Identify the blood parasite species.
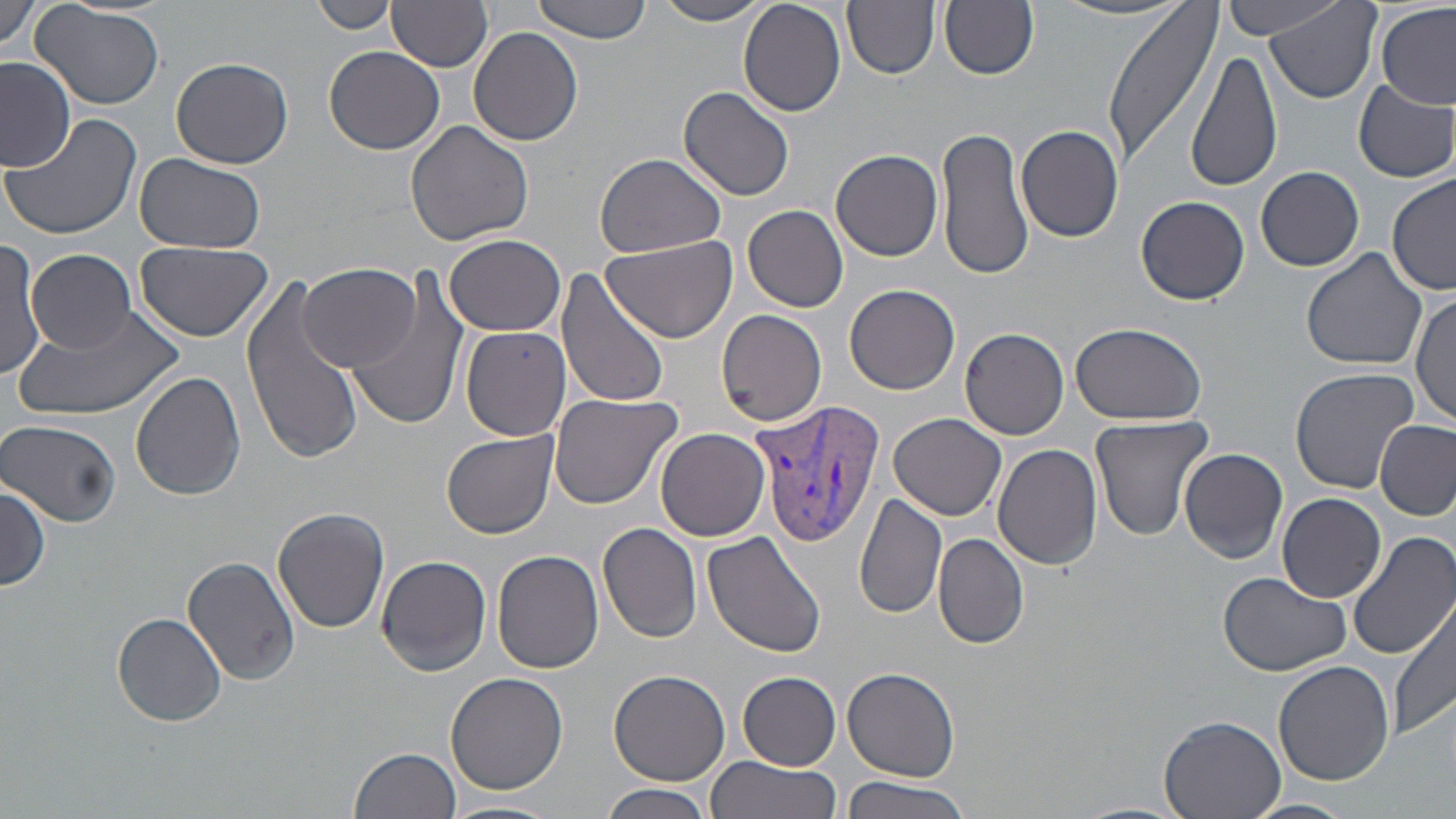
Plasmodium vivax.

Summary:
  - Coordinate format: approximate bounding boxes as (x1, y1, x2, y2) in pixels
  - Plasmodium vivax-infected red blood cell locations: (752, 396, 887, 547)
  - Uninfected red blood cell locations: (0, 0, 45, 57), (531, 0, 659, 45), (844, 0, 938, 79), (939, 0, 1040, 80), (1100, 0, 1225, 167), (1265, 0, 1383, 104), (310, 1, 397, 35), (655, 1, 770, 25), (739, 1, 846, 116), (1220, 1, 1353, 40), (1053, 2, 1189, 22), (33, 3, 165, 110), (390, 3, 493, 71), (1376, 3, 1454, 110), (468, 26, 583, 146), (324, 46, 445, 155), (1186, 50, 1284, 195), (171, 57, 293, 169), (0, 58, 76, 170), (1352, 78, 1456, 185), (678, 85, 795, 201), (3, 112, 143, 242), (403, 119, 535, 248), (936, 125, 1035, 282), (1015, 125, 1125, 243), (830, 149, 943, 261), (595, 151, 727, 258), (135, 152, 265, 253), (1256, 165, 1364, 272), (1386, 175, 1456, 296), (1137, 196, 1250, 305), (743, 204, 849, 313), (445, 234, 566, 337), (602, 234, 735, 344), (0, 240, 45, 381), (133, 241, 274, 340), (0, 245, 95, 365), (1301, 248, 1428, 371), (30, 249, 135, 351), (297, 262, 422, 372), (348, 269, 474, 433), (557, 271, 672, 409), (237, 272, 364, 463), (845, 284, 959, 394), (1411, 292, 1455, 429), (16, 305, 182, 418), (715, 308, 827, 426), (1069, 321, 1208, 425), (459, 325, 570, 442), (960, 327, 1068, 439), (1289, 367, 1422, 496), (131, 370, 246, 499), (547, 391, 683, 511), (889, 413, 1006, 521), (1088, 414, 1213, 541), (2, 419, 123, 527), (1375, 419, 1455, 522), (657, 428, 770, 540), (441, 431, 558, 540), (992, 442, 1103, 571), (1178, 447, 1288, 564), (0, 482, 49, 593), (854, 493, 947, 623), (1278, 493, 1388, 603), (273, 507, 391, 633), (599, 523, 702, 643), (1349, 529, 1456, 662), (701, 531, 826, 659), (932, 532, 1029, 650), (492, 550, 604, 675), (376, 554, 492, 677), (183, 555, 303, 686), (1216, 570, 1353, 674), (1388, 596, 1456, 742), (113, 611, 228, 726), (1272, 661, 1396, 788), (842, 667, 962, 782), (608, 669, 730, 788), (443, 672, 567, 795), (738, 672, 841, 768), (1159, 713, 1287, 819), (349, 746, 462, 819), (702, 755, 842, 819), (837, 776, 975, 819), (600, 783, 717, 819), (1242, 797, 1356, 819), (442, 801, 562, 819)
  - Stain: May-Grünwald-Giemsa
  - Magnification: 1000x
  - Field of view: one of a larger specimen
  - Image size: 1456×819 pixels
  - Preparation: thin blood smear
  - Modality: light microscopy